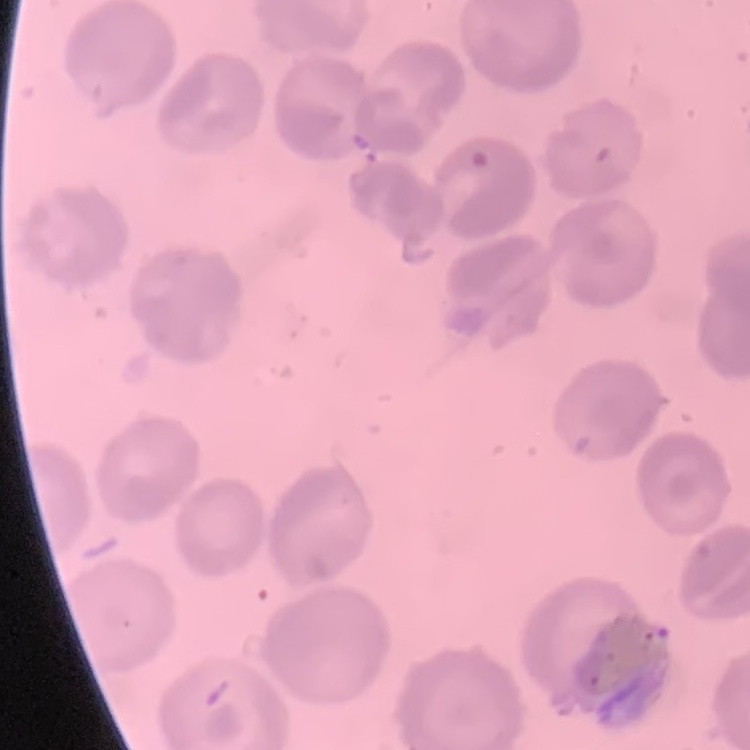 The red blood cells exhibit no rouleaux formation. Field's or Giemsa stain. Thin peripheral smear. One tile cut from a larger photomicrograph.